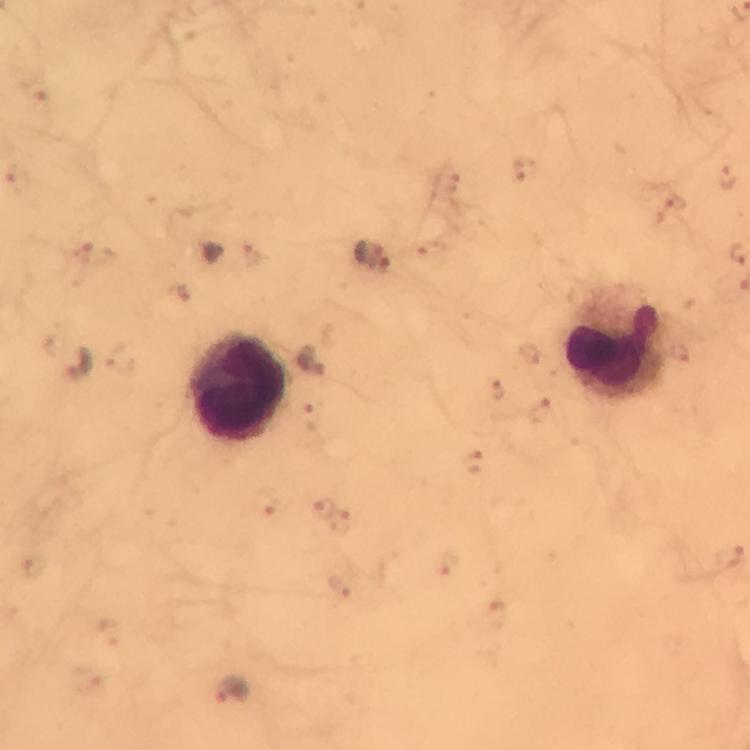 Approximate centers as {x, y} in pixels. Leukocyte locations: {617, 345}, {237, 389}. Plasmodium parasite locations: {369, 254}, {311, 361}, {79, 365}, {233, 689}. Image is 750×750 pixels. Giemsa stain. From a malaria diagnostic workup. Smartphone photograph taken through a microscope. Cropped region of a single field of view. Thick blood film. 100x magnification. Immersion oil was used.